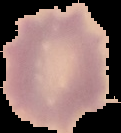
Summary:
  - Image type: cell region segmented out of the field of view; surrounding area masked to black
  - Result: negative for Plasmodium parasites
  - Preparation: thin blood film
  - Image size: 121×133 pixels